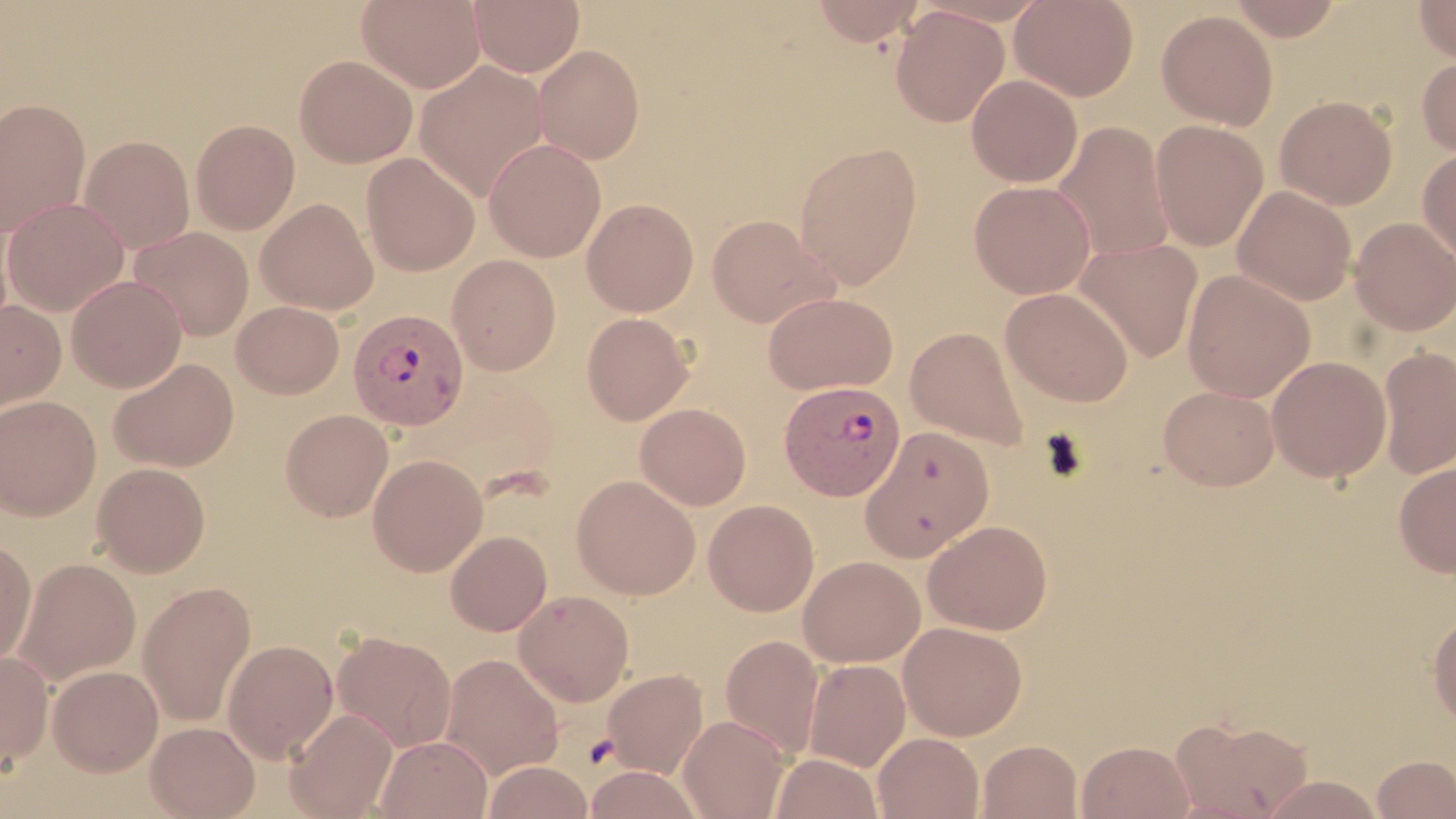

slide-level diagnosis = Plasmodium vivax
field of view = one of a larger specimen
Plasmodium vivax-infected red blood cell locations = approximate bounding boxes as [x1, y1, x2, y2] in pixels: [349, 311, 470, 433], [779, 380, 906, 500]
magnification = 1000x
modality = light microscopy
uninfected red blood cell locations = approximate bounding boxes as [x1, y1, x2, y2] in pixels: [357, 0, 486, 94], [470, 0, 584, 76], [810, 0, 924, 46], [1010, 0, 1139, 101], [1225, 0, 1345, 41], [1414, 0, 1456, 64], [890, 5, 1009, 128], [1156, 9, 1278, 129], [532, 44, 646, 164], [294, 54, 418, 168], [1416, 55, 1456, 159], [414, 61, 549, 202], [966, 74, 1083, 187], [1275, 95, 1397, 209], [0, 97, 91, 237], [190, 119, 300, 234], [1150, 120, 1268, 251], [1052, 121, 1175, 263], [79, 134, 195, 253], [484, 138, 606, 262], [793, 141, 923, 289], [1417, 146, 1456, 264], [361, 153, 480, 276], [969, 180, 1095, 299], [1232, 185, 1356, 305], [2, 198, 128, 316], [256, 198, 378, 315], [582, 198, 699, 316], [706, 214, 836, 327], [1350, 217, 1456, 335], [128, 227, 254, 341], [1074, 239, 1203, 363], [446, 254, 562, 375], [1182, 269, 1315, 402], [66, 274, 187, 393], [1001, 287, 1134, 406], [763, 292, 898, 395], [0, 299, 66, 418], [231, 300, 344, 399], [581, 312, 694, 425], [905, 327, 1029, 449], [1378, 346, 1456, 479], [1267, 355, 1391, 482], [108, 358, 240, 473], [1157, 385, 1280, 491], [0, 395, 101, 520], [635, 403, 751, 510], [280, 409, 393, 521], [860, 426, 994, 561], [368, 454, 488, 576], [1394, 461, 1456, 578], [92, 462, 210, 577], [571, 475, 700, 599], [703, 499, 819, 616], [922, 520, 1053, 635], [445, 530, 552, 636], [0, 538, 36, 667], [799, 555, 925, 667], [14, 558, 140, 685], [137, 580, 256, 727], [513, 589, 634, 706], [1428, 611, 1456, 730], [898, 621, 1027, 741], [332, 630, 457, 752], [719, 634, 824, 759], [222, 639, 338, 761], [0, 650, 54, 769], [439, 653, 564, 780], [803, 659, 910, 771], [47, 665, 163, 776], [602, 668, 708, 779], [285, 708, 398, 818], [678, 714, 790, 819], [1168, 715, 1315, 819], [146, 721, 260, 818], [873, 732, 984, 819], [375, 734, 492, 818], [977, 739, 1082, 819], [1076, 740, 1193, 818], [771, 752, 882, 818], [1372, 754, 1456, 818], [482, 760, 593, 819], [584, 766, 704, 819], [1260, 774, 1384, 818]
image size = 1456×819 pixels
stain = May-Grünwald-Giemsa
preparation = thin blood film